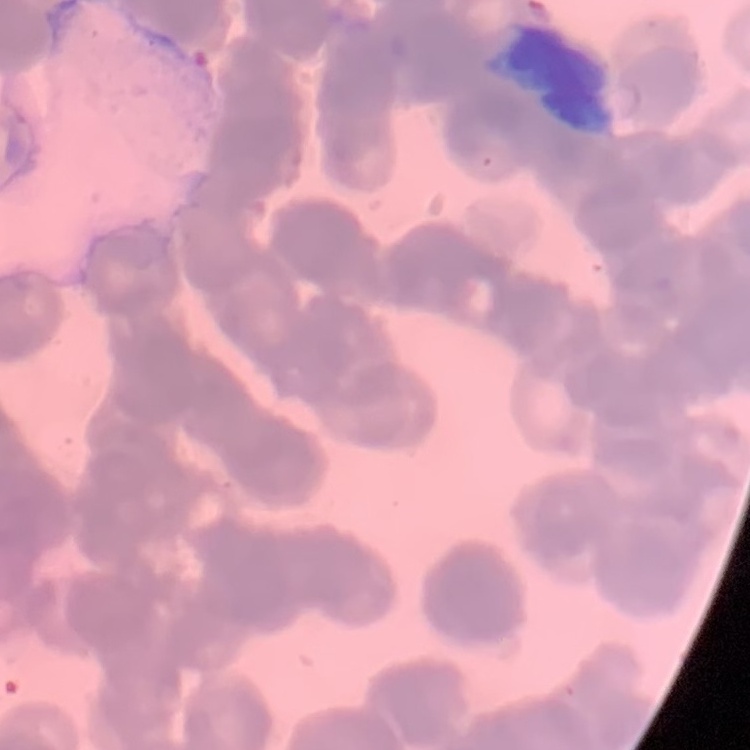

Summary:
  - Red blood cell morphology: rouleaux formation
  - Preparation: thin blood smear
  - Image type: one tile cut from a larger photomicrograph
  - Stain: Field's or Giemsa